Give the preparation type.
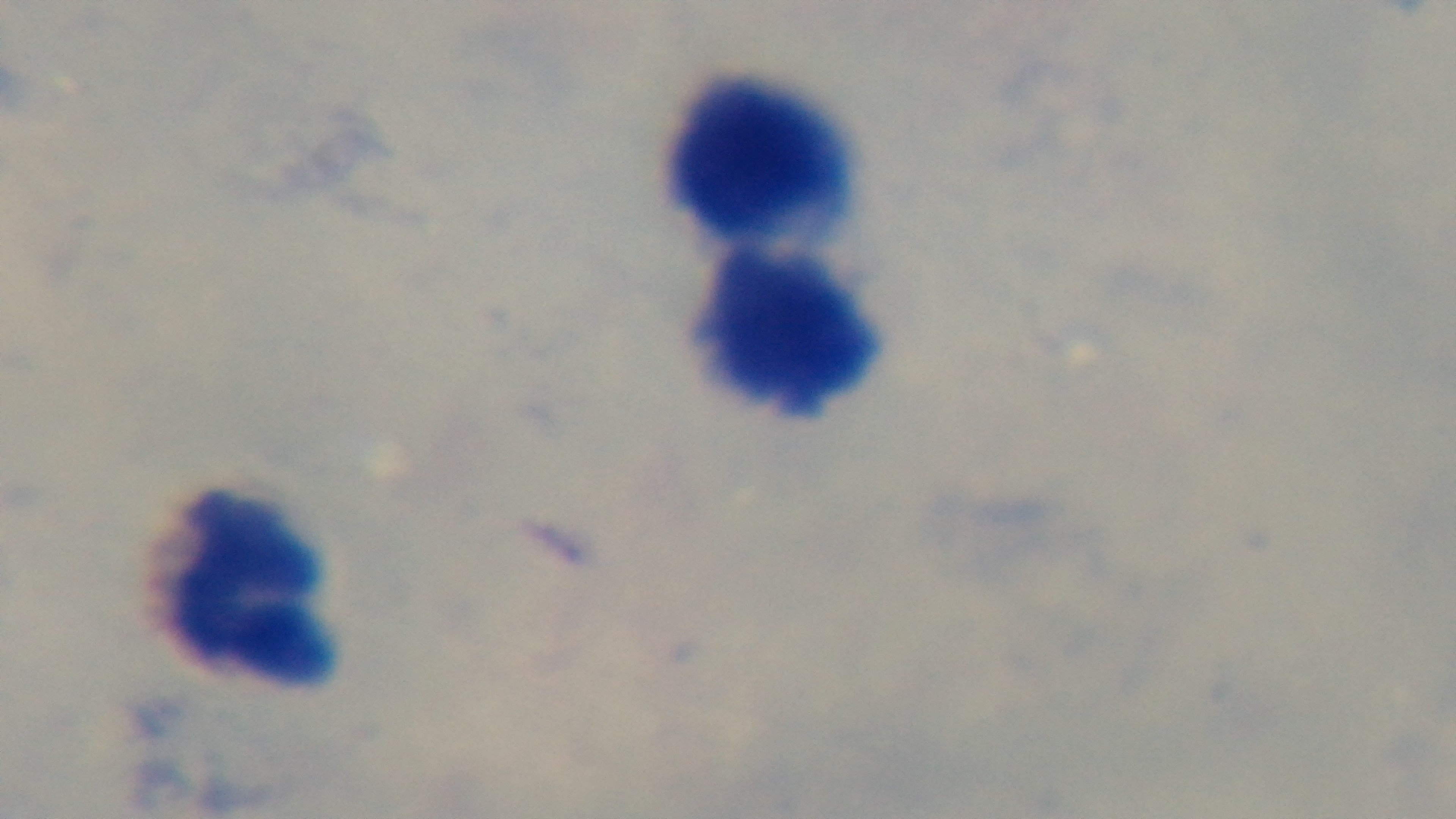
A thick smear.

Summary:
  - Malaria status: uninfected
  - Objective: 100x oil immersion
  - Field of view: one from the slide
  - Modality: light microscopy
  - Capture: mounted 4K digital camera
  - Stain: Giemsa